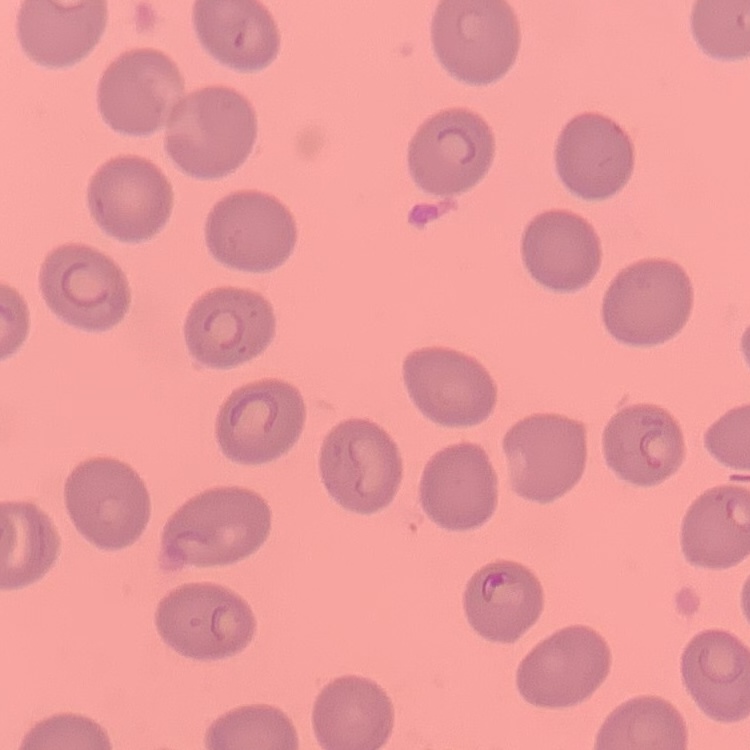

The red blood cells show no rouleaux formation. Thin blood smear. Square crop of a larger photomicrograph. Field's or Giemsa stain.